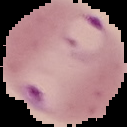 From a thin blood film. Image is 127×127 pixels. Malaria status: parasitized. The area outside the segmented cell region is set to black.